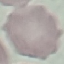

Summary:
  - Result: negative for malaria parasites
  - Stain: Giemsa
  - Image type: automatically extracted cell patch, resized to 64 × 64 pixels
  - Capture: smartphone camera at the microscope eyepiece
  - Preparation: thin blood smear